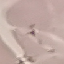
Summary:
  - Result: negative for malaria parasites
  - Image type: automatically extracted cell patch, resized to 64 × 64 pixels
  - Stain: Giemsa
  - Preparation: thin blood film
  - Capture: smartphone through the microscope eyepiece